Outline each blood parasite and name the species.
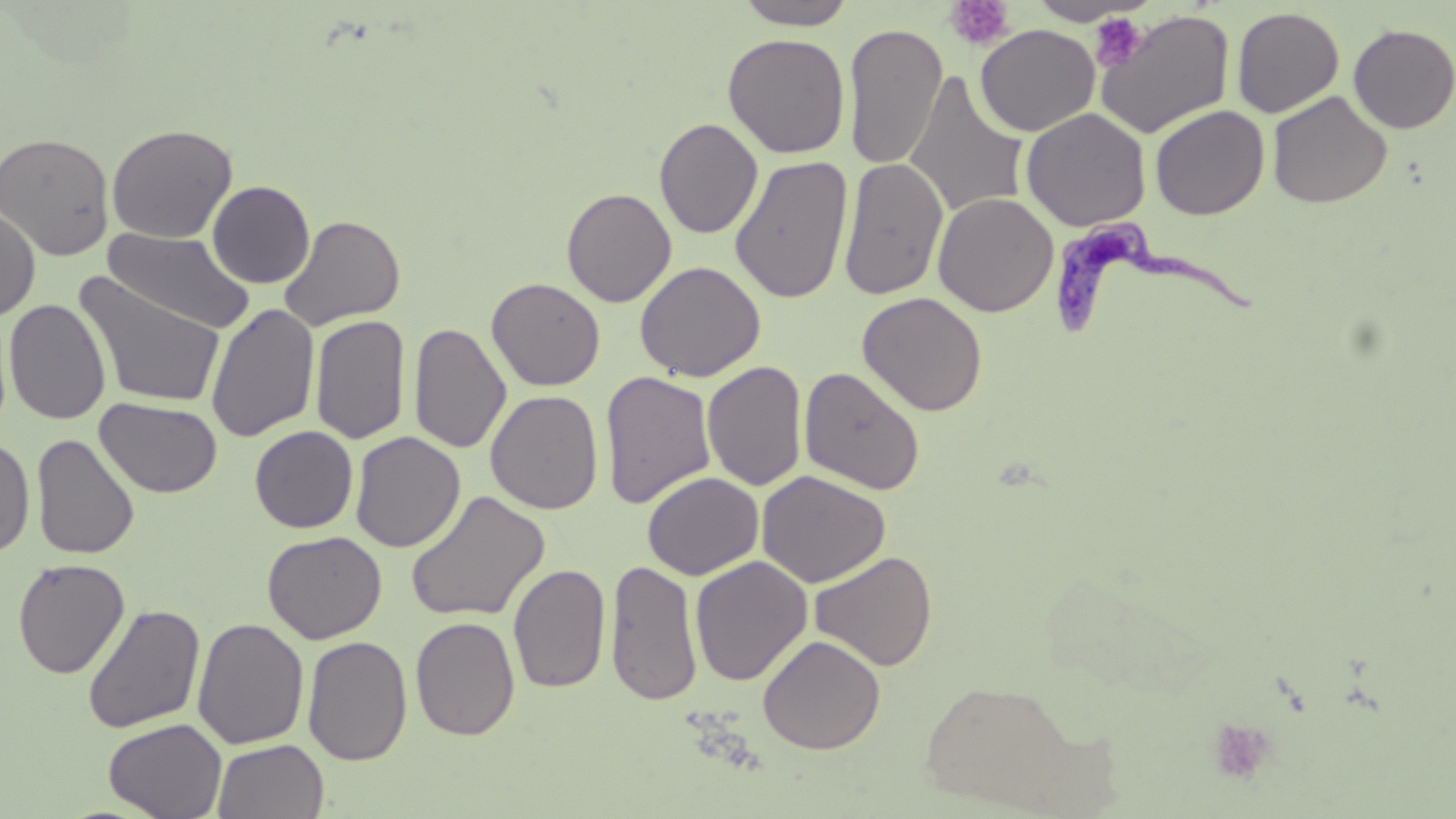

Approximate bounding boxes as named x1/y1/x2/y2 corners in pixels.
Trypanosoma brucei: (x1=1054, y1=218, x2=1271, y2=342).
No Plasmodium falciparum, Plasmodium ovale, Plasmodium malariae, Plasmodium vivax, or Babesia divergens observed.

Uninfected red blood cell locations: (x1=735, y1=0, x2=857, y2=30), (x1=1027, y1=1, x2=1150, y2=26), (x1=1232, y1=6, x2=1345, y2=118), (x1=1094, y1=9, x2=1235, y2=139), (x1=1348, y1=23, x2=1456, y2=134), (x1=843, y1=24, x2=948, y2=169), (x1=975, y1=24, x2=1100, y2=136), (x1=722, y1=32, x2=850, y2=158), (x1=904, y1=71, x2=1029, y2=220), (x1=1267, y1=90, x2=1392, y2=209), (x1=1149, y1=104, x2=1270, y2=220), (x1=1021, y1=107, x2=1152, y2=231), (x1=654, y1=117, x2=763, y2=239), (x1=106, y1=123, x2=238, y2=244), (x1=0, y1=131, x2=115, y2=261), (x1=730, y1=155, x2=853, y2=304), (x1=838, y1=156, x2=949, y2=300), (x1=207, y1=180, x2=315, y2=288), (x1=561, y1=187, x2=677, y2=306), (x1=932, y1=191, x2=1058, y2=317), (x1=0, y1=207, x2=40, y2=322), (x1=280, y1=214, x2=406, y2=331), (x1=103, y1=227, x2=255, y2=336), (x1=635, y1=261, x2=766, y2=381), (x1=74, y1=272, x2=227, y2=409), (x1=486, y1=276, x2=606, y2=391), (x1=857, y1=291, x2=988, y2=416), (x1=4, y1=299, x2=111, y2=425), (x1=205, y1=303, x2=320, y2=443), (x1=310, y1=314, x2=410, y2=445), (x1=409, y1=322, x2=511, y2=454), (x1=702, y1=361, x2=807, y2=491), (x1=799, y1=366, x2=926, y2=495), (x1=599, y1=370, x2=717, y2=509), (x1=485, y1=389, x2=603, y2=514), (x1=95, y1=398, x2=223, y2=498), (x1=250, y1=426, x2=359, y2=533), (x1=350, y1=431, x2=466, y2=553), (x1=31, y1=433, x2=140, y2=559), (x1=0, y1=438, x2=35, y2=558), (x1=756, y1=470, x2=890, y2=588), (x1=643, y1=472, x2=763, y2=580), (x1=405, y1=489, x2=550, y2=623), (x1=262, y1=530, x2=387, y2=644), (x1=809, y1=550, x2=938, y2=671), (x1=690, y1=555, x2=813, y2=687), (x1=12, y1=557, x2=130, y2=679), (x1=604, y1=559, x2=703, y2=706), (x1=508, y1=562, x2=611, y2=694), (x1=82, y1=603, x2=205, y2=734), (x1=410, y1=616, x2=520, y2=741), (x1=192, y1=617, x2=309, y2=750), (x1=758, y1=634, x2=885, y2=754), (x1=302, y1=635, x2=413, y2=765), (x1=916, y1=678, x2=1093, y2=812), (x1=103, y1=718, x2=227, y2=819), (x1=213, y1=739, x2=329, y2=819). Platelet locations: (x1=945, y1=0, x2=1014, y2=50), (x1=1090, y1=13, x2=1149, y2=71), (x1=1207, y1=718, x2=1278, y2=787). Slide-level diagnosis: Trypanosoma brucei. Image is 1456×819 pixels. Single field of view. May-Grünwald-Giemsa-stained preparation. Light microscopy. Captured at 1000x magnification. Thin blood film.